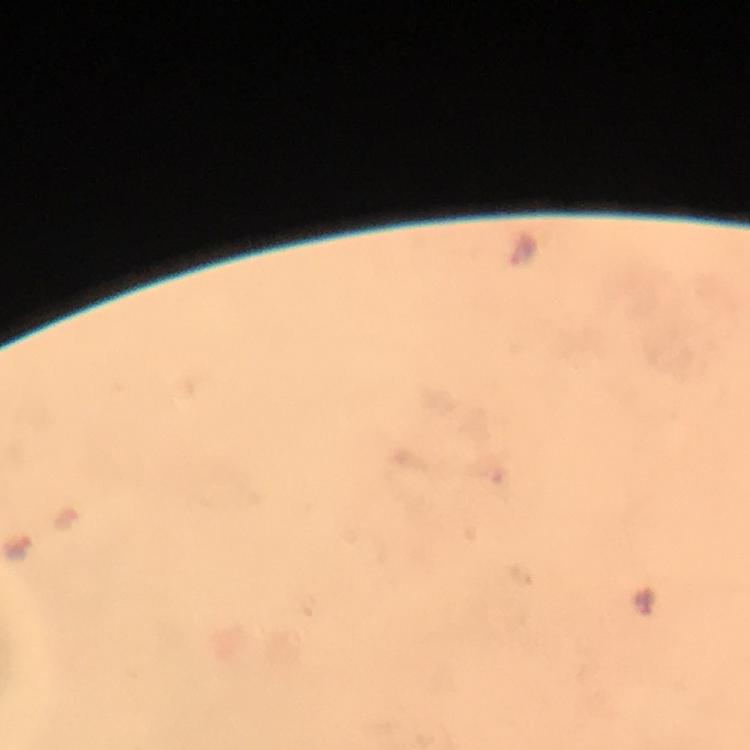

Approximate object centers, in pixels from the top-left corner. Plasmodium parasite locations: (x=18, y=544). Immersion oil was used. Photographed with a smartphone mounted on the microscope. Image is 750×750 pixels. 100x magnification. Cropped region of a single field of view. Giemsa stain. From a diagnostic examination for malaria. Thick blood film.